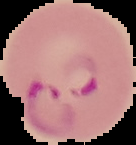
Summary:
  - Preparation: thin blood smear
  - Image size: 136×145 pixels
  - Image type: segmented cell region on a black background
  - Result: Plasmodium parasites identified